Report the malaria status of this cell.
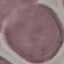
Uninfected.

Summary:
  - Stain: Giemsa
  - Capture: smartphone camera at the microscope eyepiece
  - Image type: cell patch, automatically extracted from a larger field of view and resized to 64 × 64 pixels
  - Preparation: thin blood smear